Name the parasite shown.
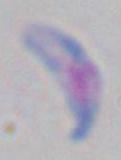

This is Toxoplasma gondii.

Micrograph. Captured at 1000x magnification.